Assess this cell for malaria.
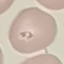
It is parasitized.

Acquired by smartphone through the microscope eyepiece. Thin blood film. Automatically extracted cell patch, resized to 64 × 64 pixels. Giemsa-stained preparation.